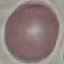

Malaria status: uninfected. Cell patch, automatically extracted from a larger field of view and resized to 64 × 64 pixels. Thin smear of blood. Giemsa stain. Acquired by smartphone through the microscope eyepiece.